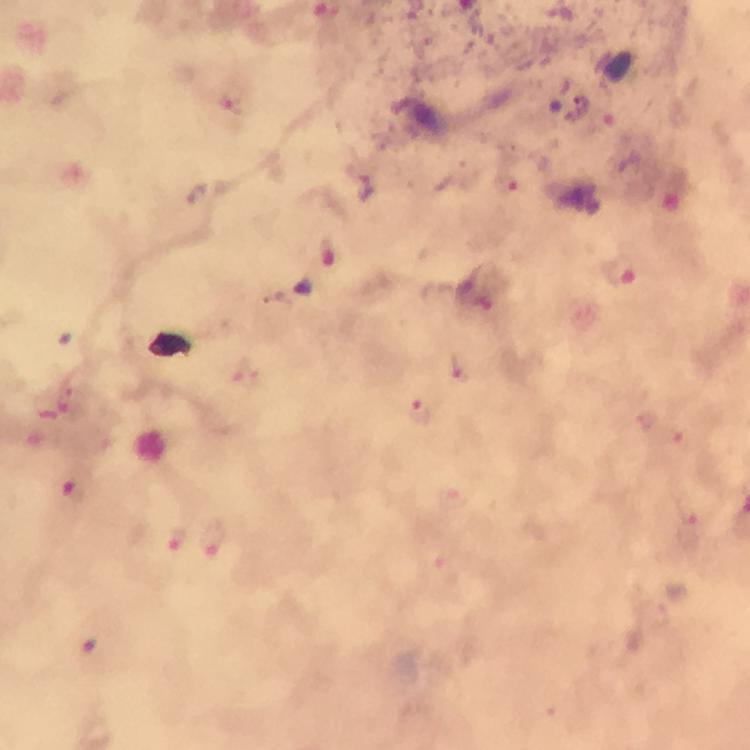
immersion_oil: used
image_size: 750×750 pixels
stain: Giemsa
capture: smartphone mounted on the microscope
magnification: 100x
cropped_from: one field of view
plasmodium_parasite_locations: 'approximate centers as (x, y) in pixels: (230, 98), (329, 250), (620, 273), (457, 364), (419, 403), (670, 437), (75, 494), (690, 525), (179, 537), (212, 539)'
preparation: thick blood smear
context: from a diagnostic examination for malaria